Assess this cell for malaria.
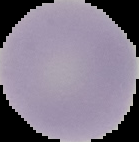

It is uninfected.

Summary:
  - Image type: segmented cell region on a black background
  - Preparation: thin blood smear
  - Image size: 139×142 pixels